Assess the morphology of the erythrocytes.
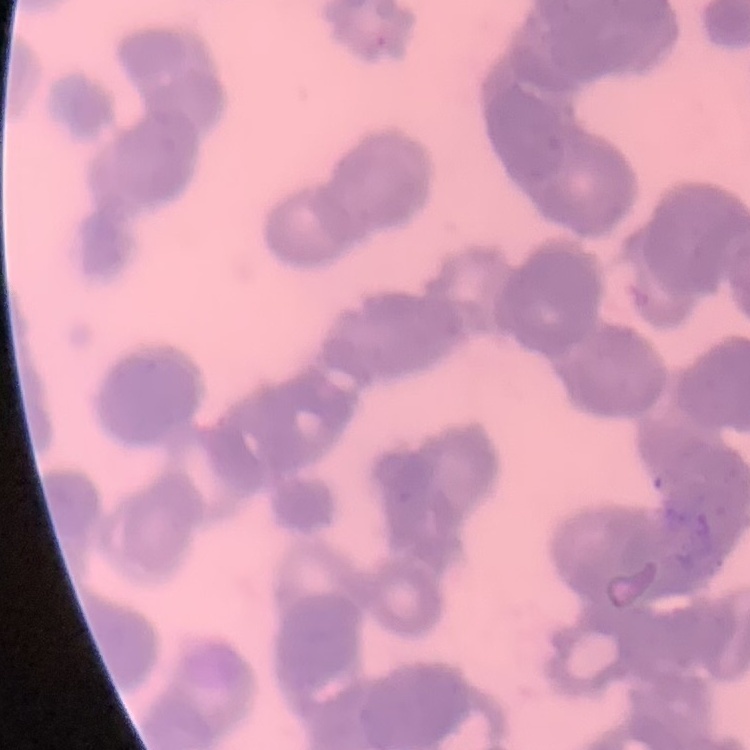
Rouleaux formation.

{
  "stain": "Field's or Giemsa",
  "image_type": "one tile cut from a larger photomicrograph",
  "preparation": "thin blood film"
}